Point out each malaria parasite.
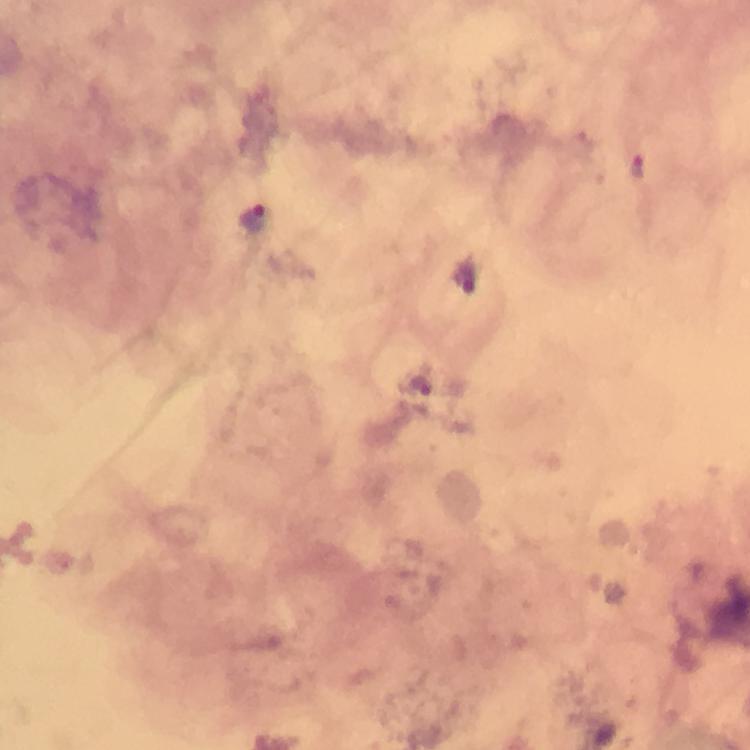
Approximate centers as (x, y) in pixels.
Malaria parasites: (640, 165), (256, 216), (419, 385).

Summary:
  - Cropped from: a single field of view
  - Preparation: thick smear
  - Capture: smartphone camera through the microscope
  - Stain: Giemsa
  - Context: from a diagnostic examination for malaria
  - Immersion oil: applied
  - Magnification: 100x
  - Image size: 750×750 pixels